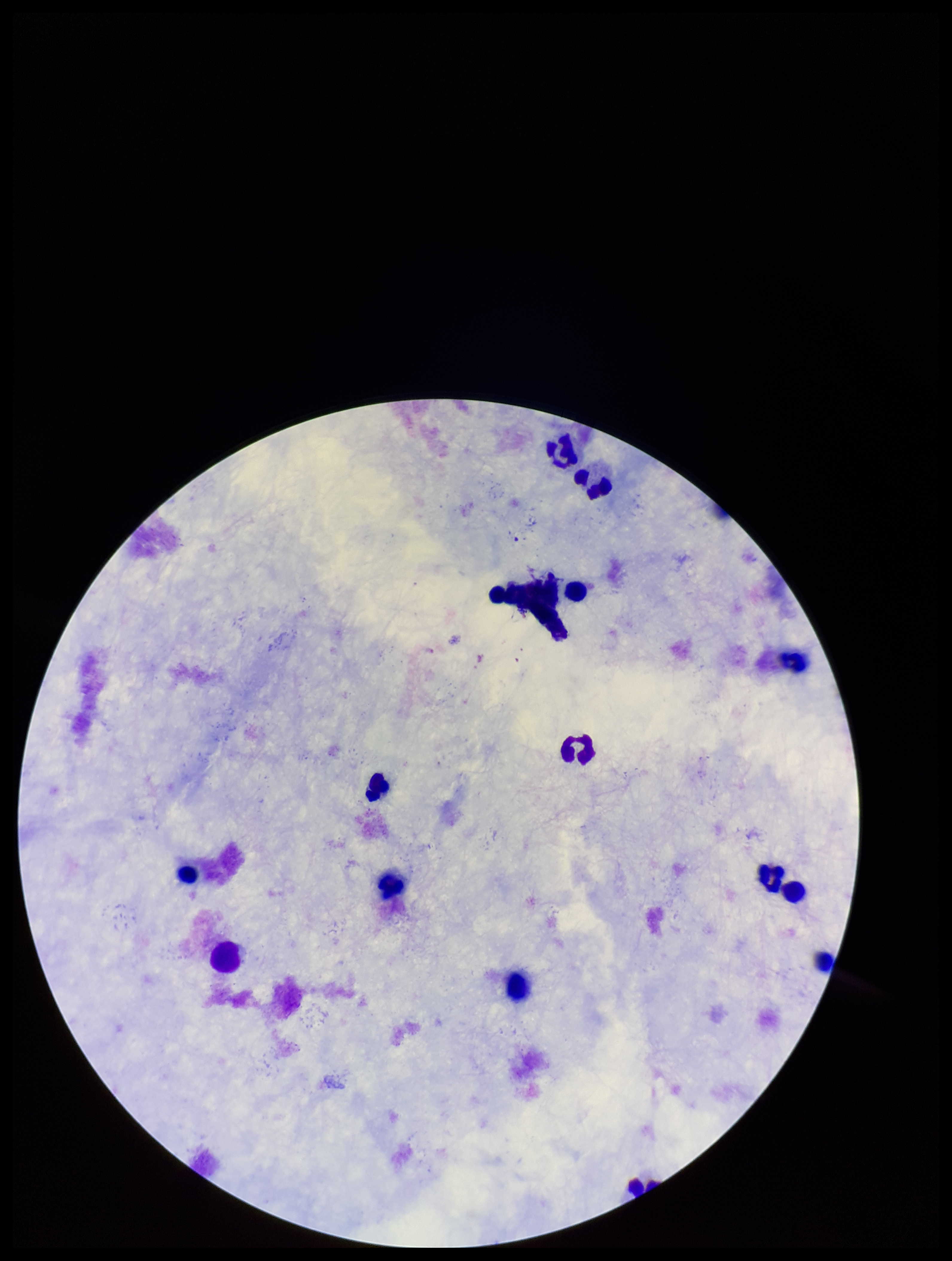

Summary:
  - Patient malaria status: negative
  - Leukocyte count: 12
  - Field of view: one from this slide
  - Plasmodium parasites: none identified
  - Stain: Giemsa
  - Capture: smartphone photograph through the microscope eyepiece
  - Parasite count: 0
  - Image size: 952×1261 pixels
  - Preparation: thick